Classify this cell by malaria status.
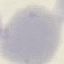

Uninfected.

Summary:
  - Stain: Giemsa
  - Capture: smartphone camera at the microscope eyepiece
  - Image type: cell patch, automatically extracted from a larger field of view and resized to 64 × 64 pixels
  - Preparation: thin blood smear